Assess this cell for malaria.
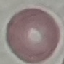
It is uninfected.

preparation: thin blood film
capture: smartphone through the microscope eyepiece
image_type: automatically extracted cell patch, resized to 64 × 64 pixels
stain: Giemsa